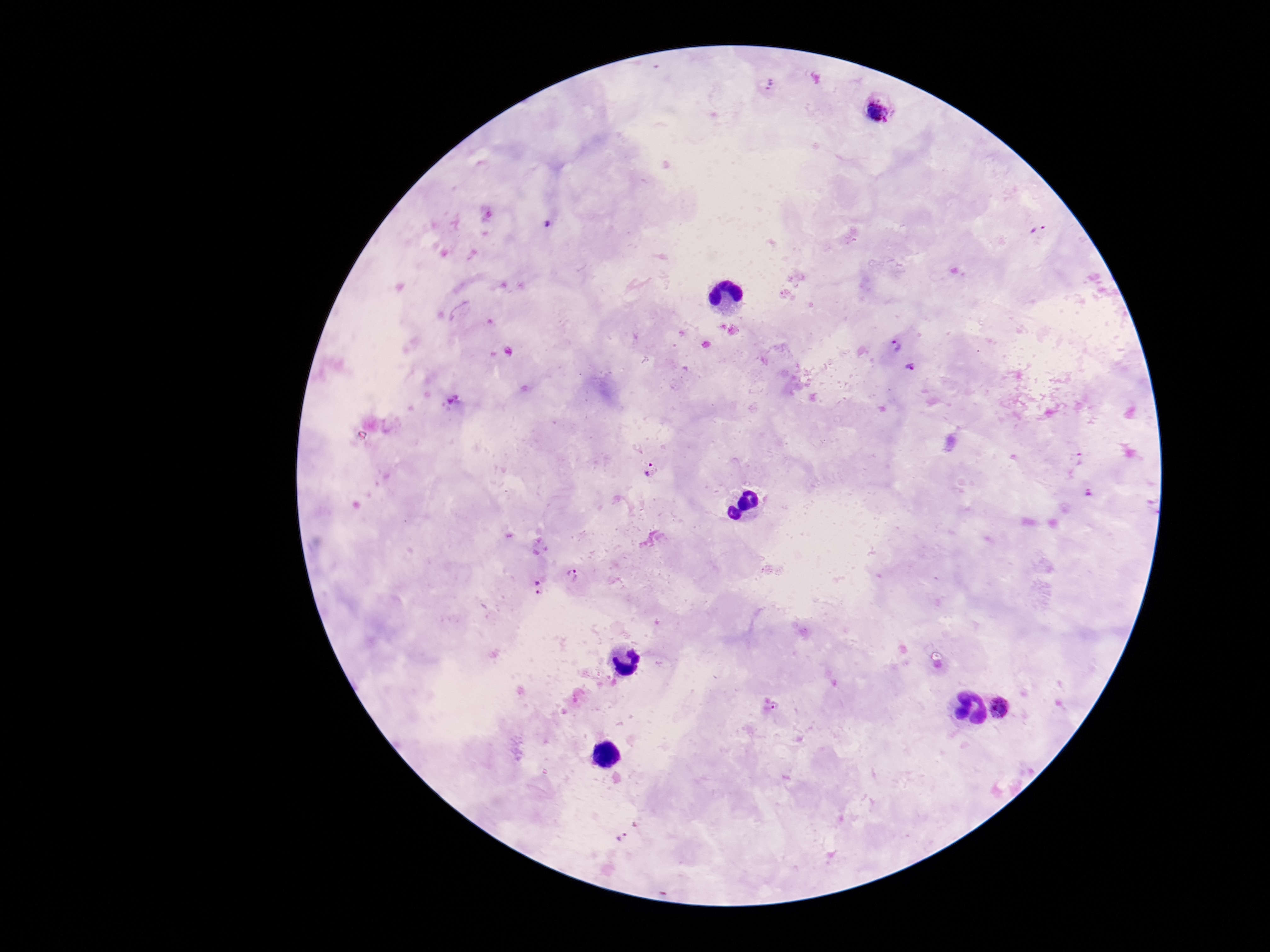

Approximate centers as (x, y) in pixels. Plasmodium parasite locations: (768, 86), (880, 108), (549, 224), (1038, 228), (896, 345), (910, 368), (651, 469), (1087, 491), (572, 575), (538, 587), (775, 707), (1000, 708), (623, 838). Patient malaria status: positive. Smartphone photograph taken through the microscope eyepiece. Image is 1270×952 pixels. Thick peripheral-blood smear. Single field of view. 100x magnification. Giemsa stain.